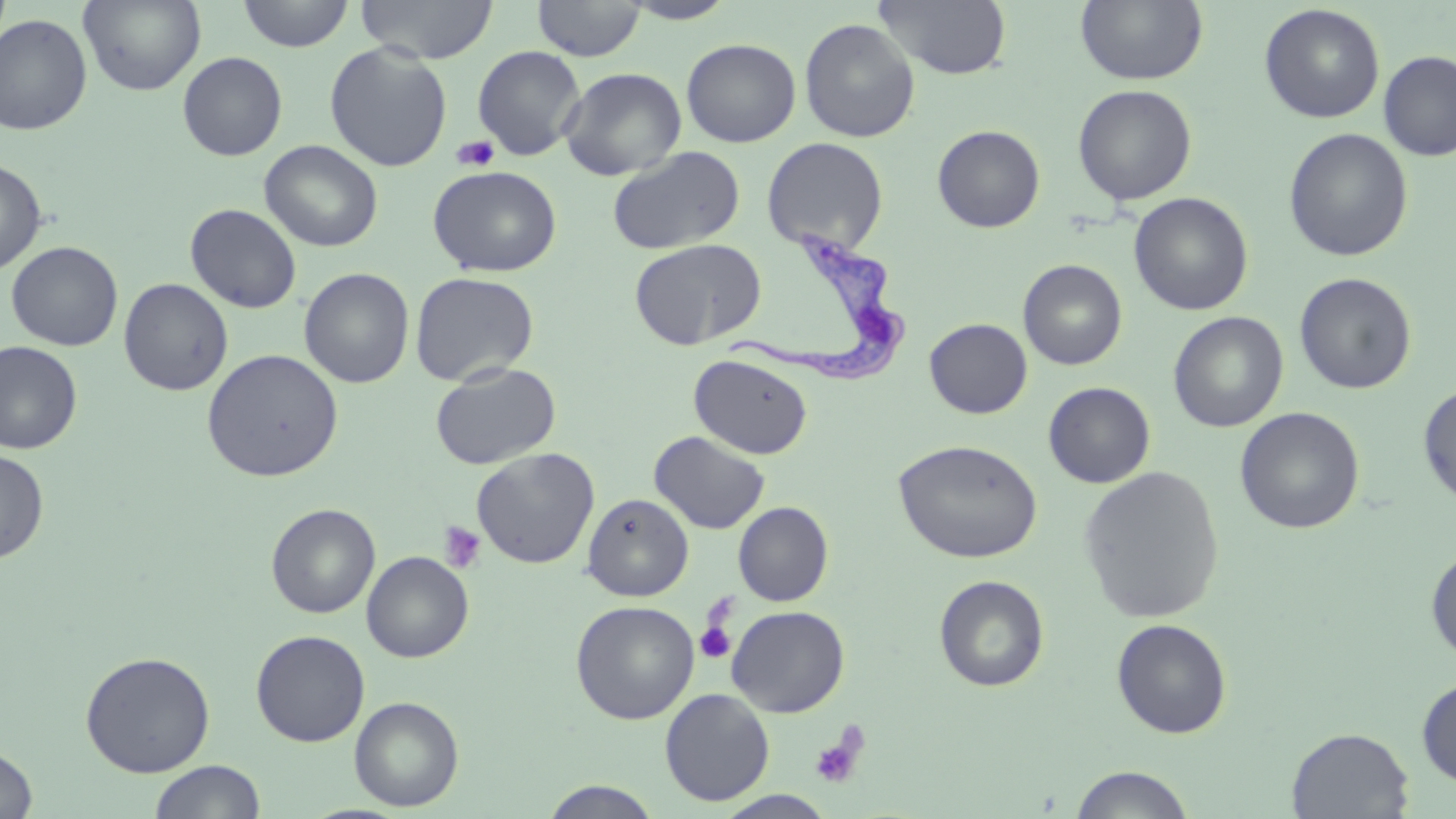
slide-level diagnosis = Trypanosoma brucei
platelet locations = approximate bounding boxes as (x1, y1, x2, y2) in pixels: (452, 135, 500, 172), (437, 520, 486, 573), (695, 614, 738, 665), (809, 727, 867, 790)
magnification = 1000x
Trypanosoma brucei locations = approximate bounding boxes as (x1, y1, x2, y2) in pixels: (727, 226, 908, 385)
field of view = one of a larger specimen
stain = May-Grünwald-Giemsa
modality = light microscopy
uninfected red blood cell locations = approximate bounding boxes as (x1, y1, x2, y2) in pixels: (78, 0, 206, 96), (237, 0, 355, 52), (356, 0, 498, 64), (533, 0, 644, 61), (873, 0, 1013, 80), (1075, 0, 1209, 86), (619, 1, 739, 24), (1259, 4, 1385, 123), (0, 13, 93, 135), (799, 17, 920, 142), (681, 38, 801, 147), (324, 42, 453, 171), (472, 45, 587, 160), (1377, 50, 1456, 161), (178, 51, 288, 161), (559, 67, 687, 181), (1072, 84, 1197, 206), (932, 125, 1045, 232), (1283, 128, 1413, 262), (762, 137, 889, 255), (259, 140, 383, 252), (606, 146, 745, 255), (0, 157, 47, 276), (427, 164, 562, 277), (1129, 192, 1253, 316), (185, 203, 302, 313), (629, 238, 767, 350), (7, 241, 123, 351), (1018, 259, 1127, 370), (299, 267, 415, 388), (410, 271, 539, 386), (1294, 272, 1417, 395), (118, 278, 233, 396), (1168, 311, 1288, 432), (924, 318, 1032, 419), (0, 341, 82, 454), (201, 348, 343, 483), (689, 353, 813, 459), (430, 361, 561, 470), (1043, 382, 1155, 488), (1418, 382, 1456, 508), (1235, 407, 1365, 534), (649, 431, 770, 534), (893, 439, 1042, 563), (0, 448, 49, 564), (471, 448, 599, 569), (1078, 466, 1224, 624), (583, 493, 694, 601), (733, 502, 833, 606), (266, 503, 380, 618), (1426, 546, 1456, 663), (361, 551, 474, 662), (933, 575, 1050, 692), (571, 600, 700, 724), (726, 605, 850, 717), (1111, 618, 1232, 739), (251, 629, 370, 747), (79, 650, 216, 777), (1416, 675, 1456, 787), (659, 688, 775, 806), (349, 696, 464, 811), (1287, 726, 1414, 818), (0, 745, 38, 818), (149, 760, 265, 819), (1068, 764, 1197, 819), (540, 780, 663, 819), (714, 790, 838, 818)
image size = 1456×819 pixels
preparation = thin blood film